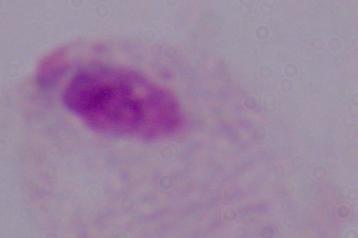
modality: photomicrograph
magnification: 1000x
identification: trichomonad